Classify this cell by malaria status.
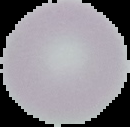
It is uninfected.

Image is 130×127 pixels. From a thin blood smear. Cell region segmented out of the field of view; the surrounding area is masked to black.